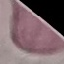

Malaria status: uninfected. Automatically extracted cell patch, resized to 64 × 64 pixels. Giemsa-stained preparation. Thin blood film. Photographed with a smartphone camera at the microscope eyepiece.